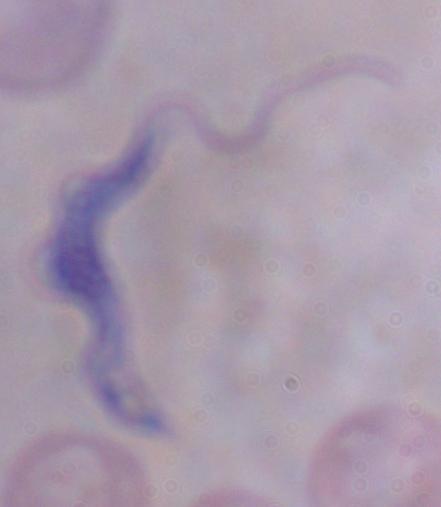 Micrograph. A trypanosome is shown. Captured at 1000x magnification.